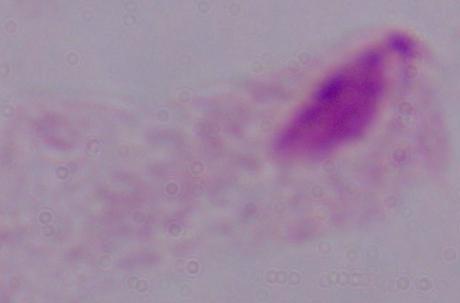
{
  "magnification": "1000x",
  "modality": "photomicrograph",
  "identification": "trichomonad"
}